Give the position of every Plasmodium parasite and every leukocyte.
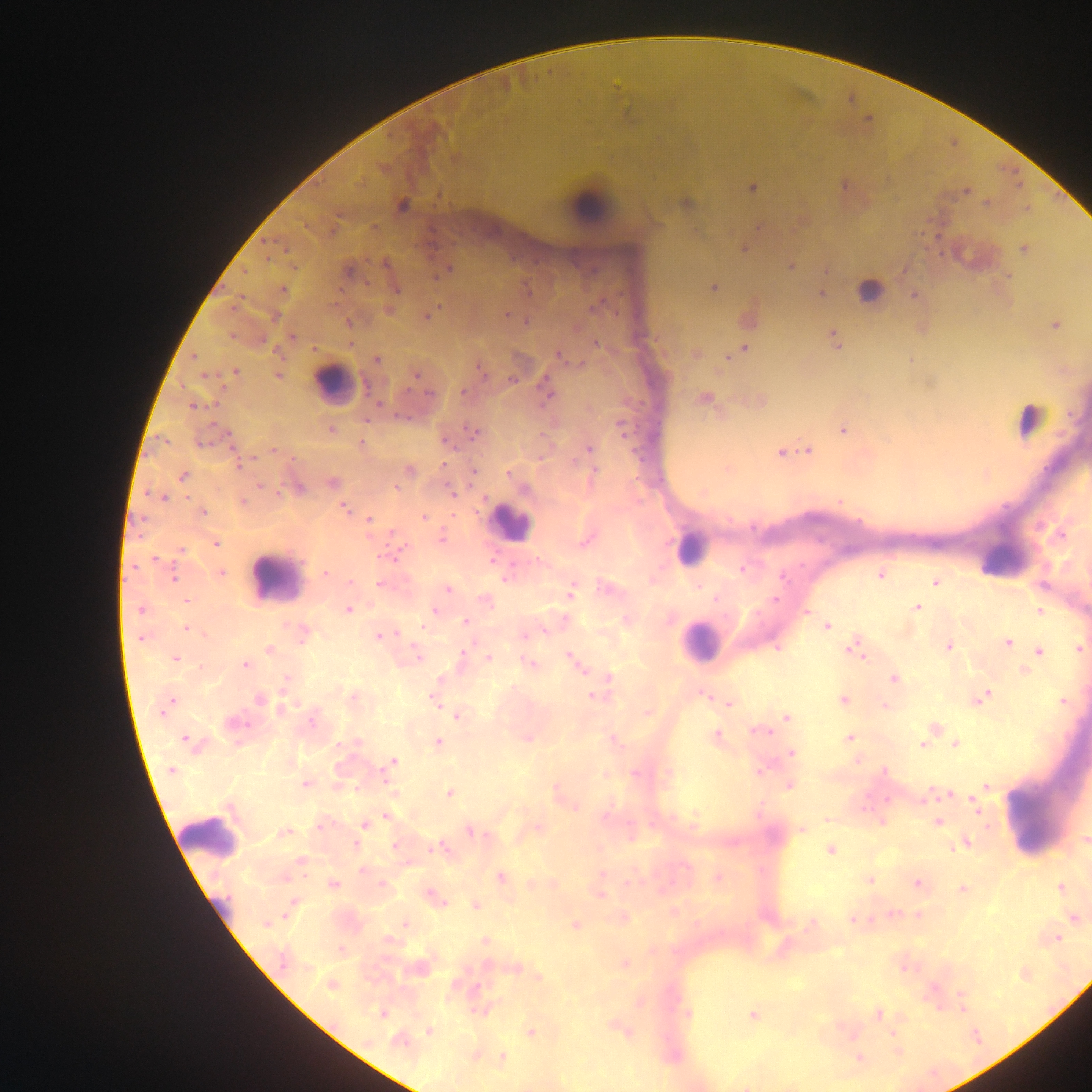

Approximate centers as (x, y) in pixels.
Plasmodium parasites: (383, 167), (843, 186), (752, 187), (966, 191), (686, 202), (986, 203), (402, 205), (759, 227), (744, 248), (1024, 248), (791, 265), (447, 269), (348, 270), (827, 270), (1008, 276), (713, 287), (395, 288), (283, 290), (820, 292), (914, 295), (390, 310), (507, 314), (426, 315), (526, 321), (348, 322), (1054, 324), (292, 337), (834, 338), (596, 344), (744, 348), (695, 353), (559, 354), (376, 359), (909, 360), (481, 370), (234, 372), (416, 374), (278, 375), (513, 379), (545, 388), (704, 398), (758, 401), (193, 405), (622, 427), (331, 429), (843, 429), (472, 433), (361, 444), (588, 449), (807, 450), (274, 451), (781, 452), (238, 463), (727, 469), (409, 470), (473, 470), (594, 470), (509, 473), (986, 474), (183, 476), (332, 482), (298, 487), (451, 493), (163, 497), (839, 501), (242, 502), (345, 508), (202, 512), (423, 516), (369, 520), (442, 537), (586, 539), (215, 543), (180, 550), (742, 568), (220, 573), (326, 573), (880, 574), (173, 576), (506, 577), (350, 582), (935, 582), (380, 583), (447, 589), (570, 590), (186, 600), (485, 600), (916, 607), (141, 609), (348, 609), (433, 610), (1039, 611), (806, 612), (668, 618), (626, 619), (466, 622), (825, 625), (187, 628), (302, 634), (525, 634), (380, 635), (1007, 643), (855, 645), (948, 646), (1078, 648), (269, 649), (1039, 651), (417, 657), (462, 657), (488, 657), (174, 658), (573, 661), (529, 663), (244, 665), (1023, 670), (894, 678), (286, 680), (608, 680), (596, 694), (704, 694), (979, 697), (259, 698), (353, 698), (435, 699), (842, 699), (1062, 701), (729, 703), (166, 705), (884, 705), (647, 712), (458, 715), (786, 717), (235, 723), (933, 728), (758, 730), (716, 736), (525, 737), (848, 738), (613, 739), (188, 741), (437, 742), (955, 743), (923, 744), (791, 752), (390, 763), (760, 769), (172, 770), (604, 774), (668, 774), (306, 783), (789, 784), (985, 786), (557, 792), (393, 793), (449, 793), (947, 794), (926, 796), (976, 806), (575, 807), (695, 815), (385, 817), (882, 821), (938, 821), (321, 824), (364, 824), (537, 828), (801, 829), (471, 831), (283, 833), (1085, 839), (964, 842), (396, 846), (442, 848), (830, 849), (300, 862), (364, 870), (500, 876), (717, 877), (869, 880), (553, 883), (918, 883), (333, 884), (382, 885), (1059, 888), (962, 889), (600, 893), (434, 898), (292, 904), (476, 905), (673, 911), (892, 914), (918, 915), (1073, 917), (622, 918), (853, 918), (267, 923), (405, 924), (576, 924), (810, 924), (1056, 937), (485, 941), (341, 949), (623, 964), (902, 965), (513, 967), (418, 968), (1024, 973), (538, 978), (331, 984), (961, 1001), (482, 1009), (382, 1013), (687, 1013), (877, 1013), (752, 1015), (620, 1029), (430, 1030), (530, 1032), (892, 1032), (400, 1040), (898, 1051), (474, 1055), (502, 1057), (859, 1058), (747, 1085).
Leukocytes: (588, 206), (973, 256), (870, 292), (333, 385), (1028, 419), (510, 522), (688, 547), (1003, 561), (275, 578), (700, 643), (1036, 812), (209, 838).

Summary:
  - Image size: 1092×1092 pixels
  - Country: Ghana
  - Field of view: single
  - Capture: mobile-phone photograph through a microscope
  - Preparation: thick blood film